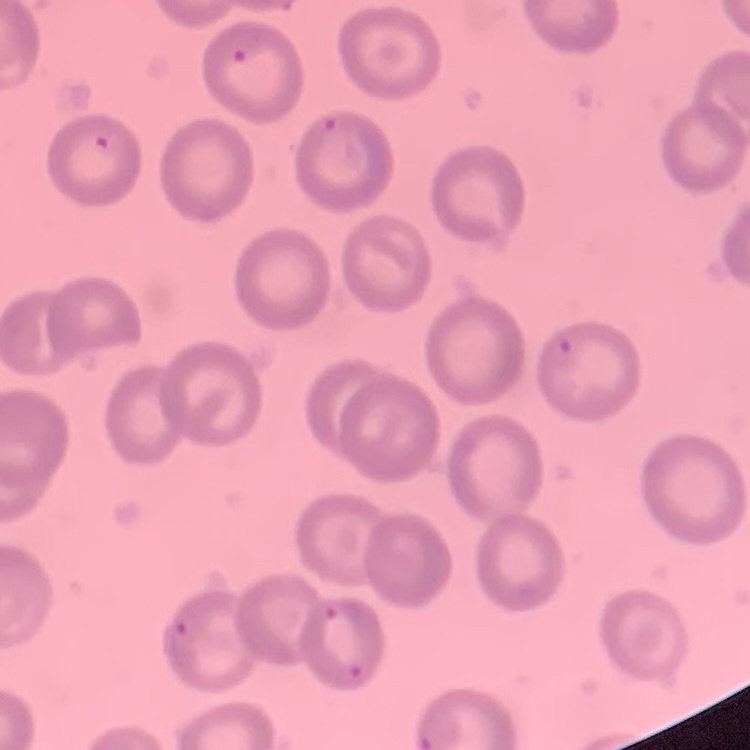

erythrocyte morphology = no rouleaux formation
stain = Field's or Giemsa
preparation = thin blood smear
image type = one tile cut from a larger photomicrograph